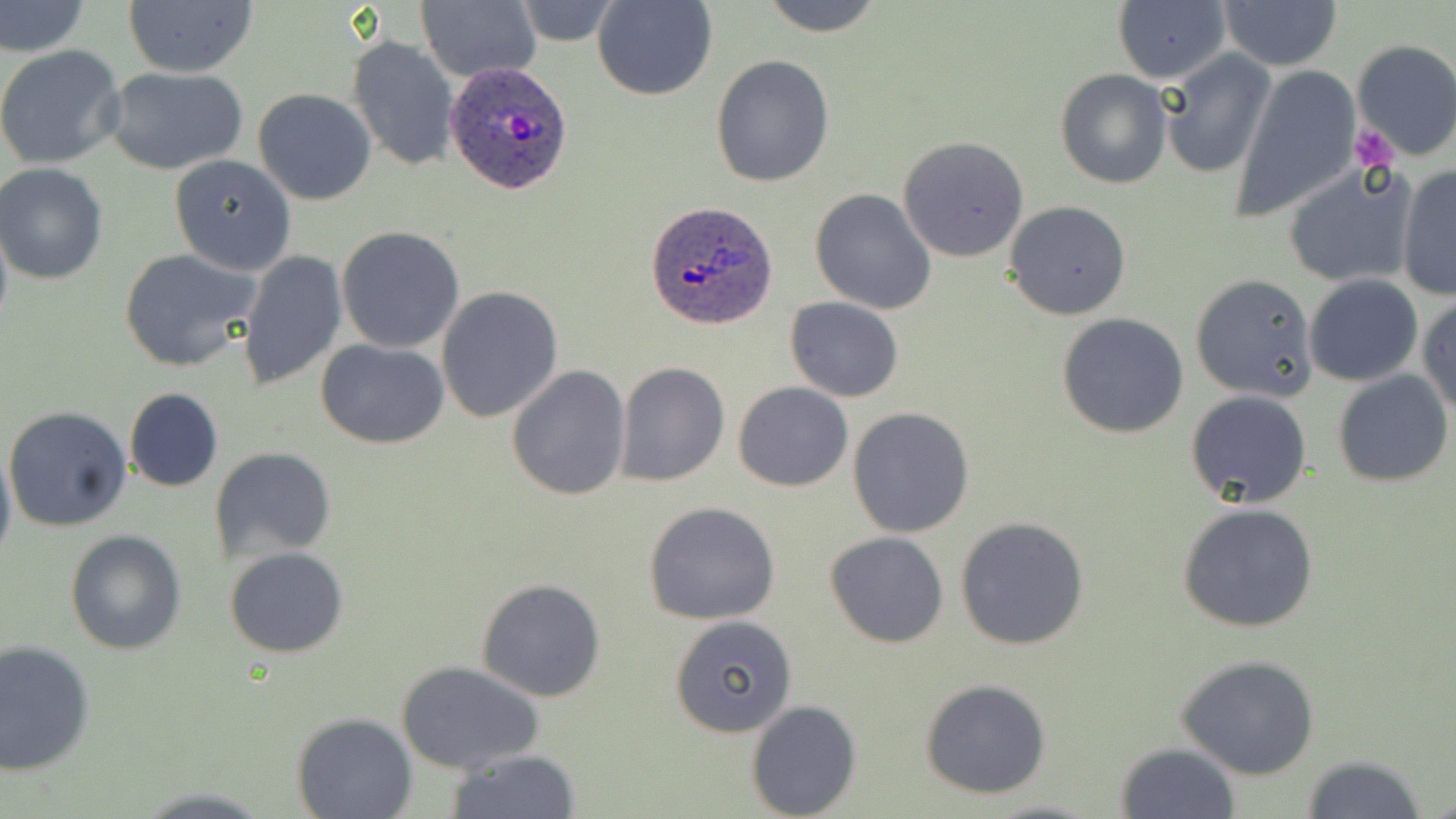
Summary:
  - Coordinate format: approximate bounding boxes as (x1,y1)-(x2,y2) corner pairs in pixels
  - Uninfected red blood cell locations: (419,0)-(541,83), (593,0)-(716,101), (757,0)-(886,37), (0,1)-(88,59), (122,1)-(257,78), (512,1)-(621,46), (1219,1)-(1342,71), (1113,3)-(1230,83), (347,35)-(459,171), (1351,40)-(1456,161), (0,44)-(126,171), (1160,51)-(1277,178), (711,56)-(834,188), (1235,65)-(1361,222), (102,66)-(248,175), (1055,68)-(1173,188), (253,89)-(377,206), (898,134)-(1030,262), (169,155)-(297,275), (1282,162)-(1417,289), (0,166)-(108,284), (1396,166)-(1456,300), (810,188)-(937,314), (1004,201)-(1131,320), (0,214)-(12,345), (336,226)-(466,354), (118,248)-(262,372), (236,249)-(348,391), (1191,274)-(1317,401), (1304,275)-(1423,387), (437,286)-(564,423), (1417,295)-(1456,419), (785,297)-(905,402), (1057,313)-(1189,439), (317,339)-(449,450), (615,362)-(730,488), (507,365)-(632,502), (1334,371)-(1453,488), (734,382)-(852,491), (123,389)-(223,493), (1186,390)-(1312,510), (4,407)-(132,532), (847,407)-(976,539), (0,443)-(16,567), (213,447)-(334,561), (642,501)-(783,625), (1177,504)-(1320,632), (955,517)-(1090,651), (65,528)-(187,655), (825,531)-(950,648), (224,546)-(349,659), (475,578)-(606,702), (670,615)-(799,738), (0,641)-(95,776), (1176,654)-(1321,779), (397,661)-(544,774), (920,678)-(1051,799), (746,699)-(862,818), (290,711)-(416,819), (1115,742)-(1240,819), (443,749)-(583,818), (1301,754)-(1428,819), (982,798)-(1106,818)
  - Platelet locations: (1352,123)-(1399,171)
  - Plasmodium ovale-infected red blood cell locations: (446,60)-(576,195), (647,200)-(780,329)
  - Slide-level diagnosis: Plasmodium ovale
  - Field of view: single
  - Image size: 1456×819 pixels
  - Stain: May-Grünwald-Giemsa
  - Modality: light microscopy
  - Preparation: thin blood smear
  - Magnification: 1000x